Describe the morphology of the erythrocytes.
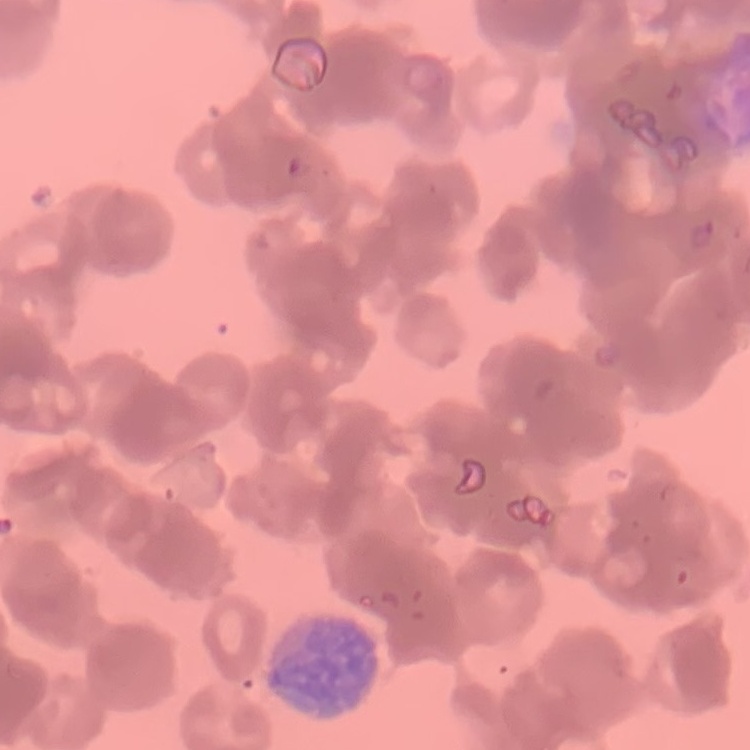
They show rouleaux formation.

{
  "stain": "Field's or Giemsa",
  "image_type": "one tile cut from a larger photomicrograph",
  "preparation": "thin peripheral smear"
}